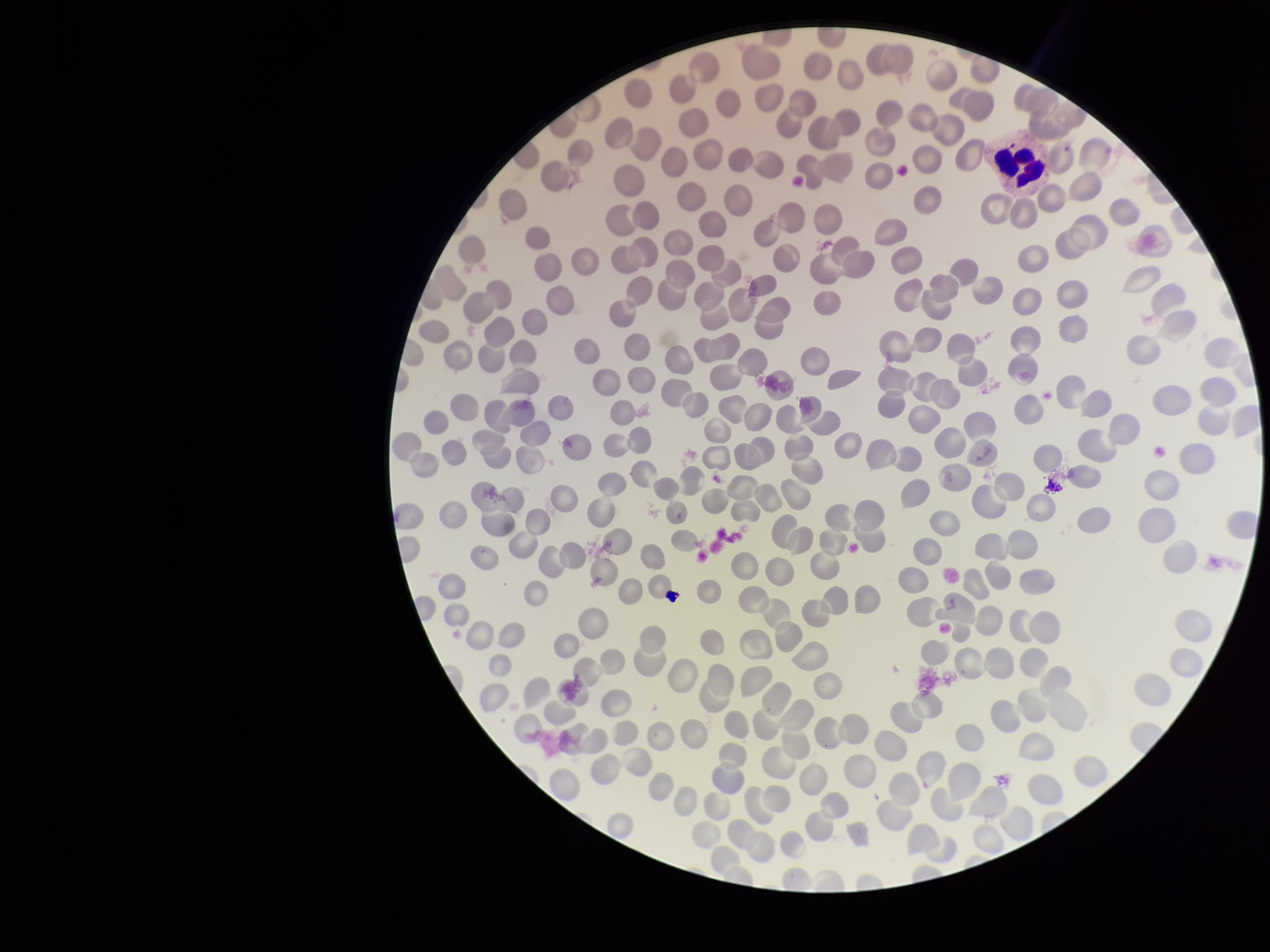 Parasitized red blood cells: none identified. Smartphone photograph taken through the eyepiece of a microscope. Preparation: thin smear. Parasitized red blood cell count: 0. Single field of view. Red blood cell count: 256. Giemsa stain. Patient malaria status: negative. Image is 1270×952 pixels.